Give the location of every parasitized red blood cell.
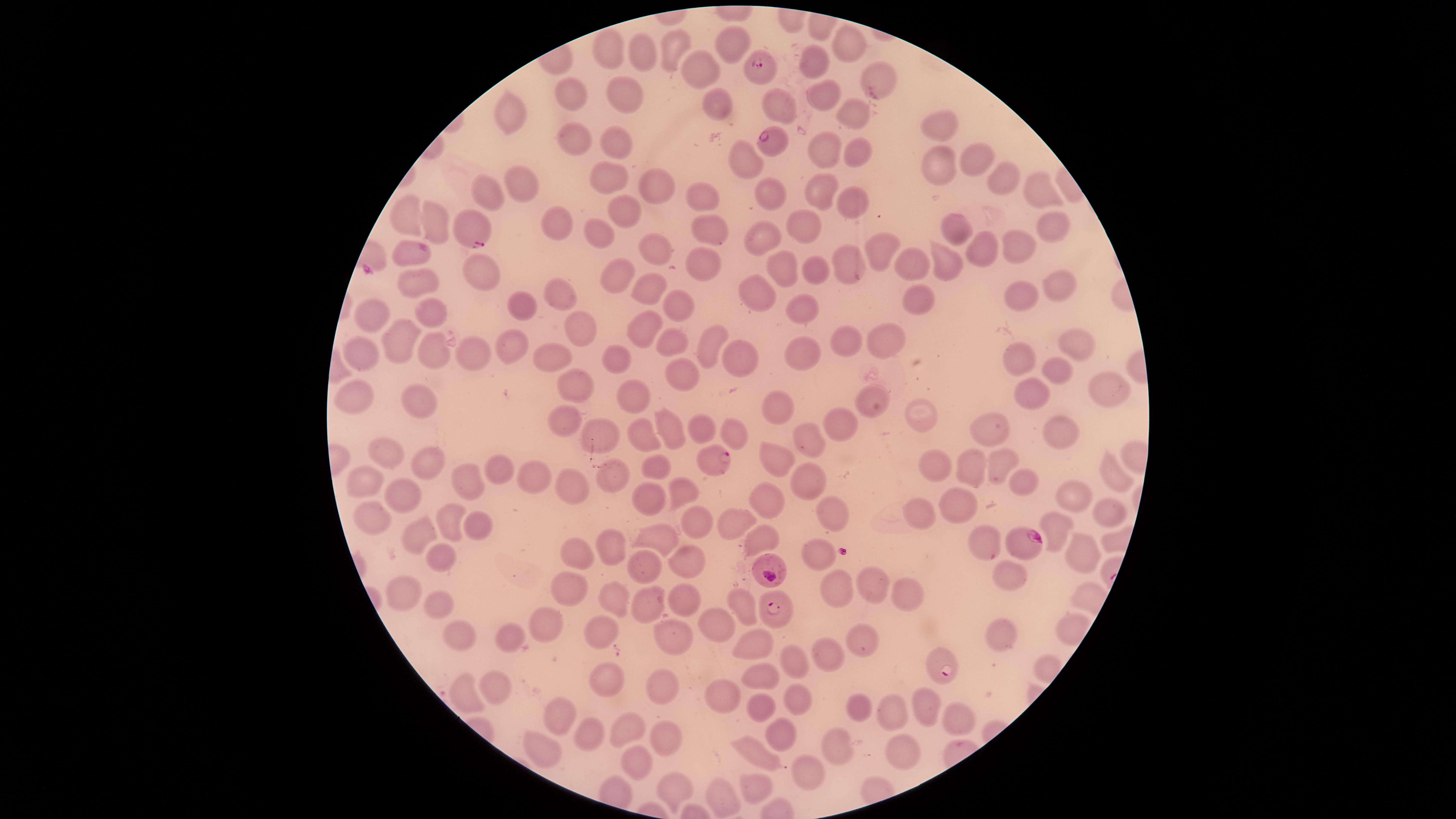

Approximate marker points as {x, y} in pixels.
Parasitized red blood cells: {762, 65}, {773, 140}, {473, 229}, {714, 459}, {1020, 541}, {773, 567}, {772, 616}, {939, 666}.

Approximate marker points as {x, y} in pixels. Uninfected red blood cells: {851, 45}, {730, 47}, {677, 48}, {608, 51}, {639, 57}, {814, 67}, {695, 73}, {871, 74}, {622, 91}, {574, 96}, {713, 97}, {822, 102}, {513, 114}, {855, 118}, {938, 124}, {571, 138}, {611, 144}, {823, 152}, {856, 153}, {743, 157}, {968, 162}, {934, 171}, {994, 174}, {514, 184}, {608, 184}, {651, 184}, {1039, 187}, {488, 189}, {824, 190}, {766, 192}, {702, 199}, {852, 201}, {619, 208}, {410, 223}, {560, 223}, {1046, 225}, {439, 226}, {804, 227}, {955, 227}, {708, 228}, {756, 235}, {603, 238}, {1019, 246}, {653, 248}, {982, 248}, {881, 250}, {406, 254}, {845, 260}, {947, 261}, {700, 262}, {783, 263}, {817, 269}, {911, 270}, {482, 276}, {618, 278}, {420, 280}, {1058, 281}, {656, 292}, {752, 294}, {1023, 295}, {561, 298}, {518, 300}, {679, 303}, {919, 306}, {803, 310}, {439, 311}, {377, 319}, {579, 323}, {645, 325}, {843, 339}, {406, 340}, {683, 341}, {885, 341}, {708, 342}, {514, 344}, {1079, 344}, {362, 349}, {433, 350}, {470, 352}, {734, 354}, {797, 356}, {619, 358}, {554, 360}, {1021, 360}, {1053, 371}, {684, 375}, {577, 383}, {1104, 387}, {353, 397}, {631, 397}, {1036, 397}, {428, 398}, {867, 398}, {920, 409}, {785, 411}, {844, 420}, {563, 423}, {669, 428}, {707, 431}, {984, 432}, {1060, 432}, {595, 435}, {735, 435}, {808, 439}, {648, 440}, {394, 457}, {782, 458}, {433, 462}, {657, 466}, {501, 467}, {1005, 468}, {938, 470}, {975, 471}, {461, 474}, {1115, 475}, {541, 477}, {615, 477}, {810, 478}, {1026, 483}, {364, 485}, {575, 487}, {681, 487}, {401, 496}, {1070, 496}, {769, 501}, {648, 503}, {957, 507}, {823, 511}, {1098, 513}, {453, 516}, {917, 516}, {372, 518}, {696, 521}, {730, 522}, {477, 524}, {1048, 524}, {421, 531}, {659, 535}, {763, 539}, {614, 542}, {983, 545}, {817, 548}, {442, 550}, {1082, 551}, {577, 555}, {686, 555}, {641, 567}, {1005, 580}, {880, 587}, {901, 590}, {402, 591}, {568, 592}, {834, 593}, {689, 598}, {646, 600}, {738, 601}, {616, 607}, {432, 608}, {719, 622}, {551, 625}, {453, 627}, {598, 628}, {673, 634}, {1001, 634}, {507, 638}, {865, 638}, {749, 644}, {828, 655}, {793, 663}, {609, 678}, {764, 678}, {497, 682}, {667, 684}, {723, 694}, {801, 694}, {462, 696}, {923, 706}, {765, 707}, {862, 710}, {560, 713}, {893, 716}, {960, 719}, {593, 731}, {631, 731}, {780, 736}, {661, 741}, {540, 746}, {842, 750}, {757, 753}, {908, 753}, {634, 758}, {812, 772}, {758, 788}, {678, 789}, {720, 798}. Thin blood smear. The visible region is circular. Smartphone photograph through the microscope eyepiece. Giemsa stain. Species: Plasmodium falciparum. Single field of view. Image is 1456×819 pixels.